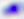
Summary:
  - Identification: Toxoplasma gondii
  - Magnification: 400x
  - Modality: micrograph